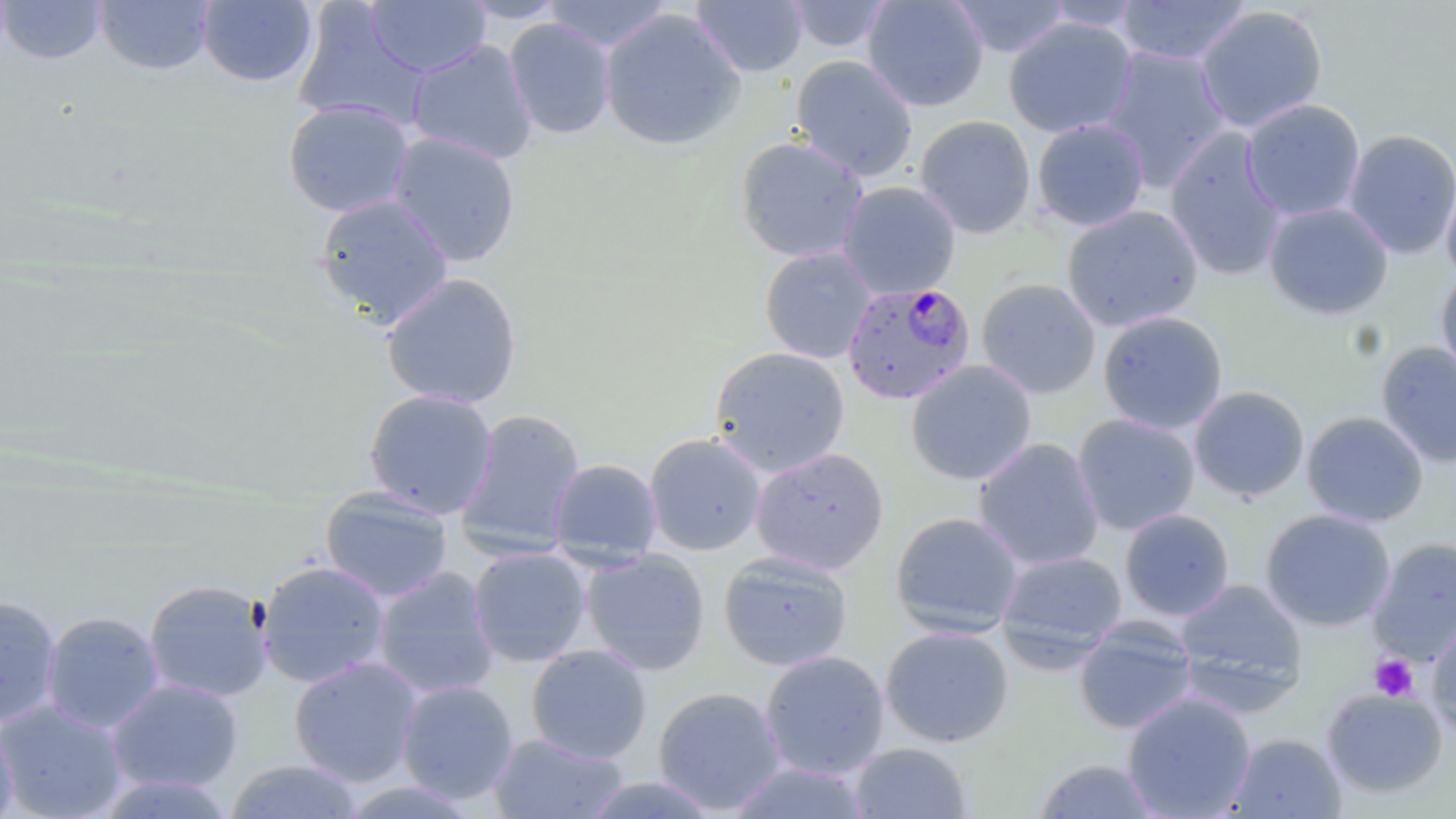 Approximate bounding boxes as (x1, y1, x2, y2) in pixels. Uninfected red blood cell locations: (0, 0, 107, 65), (458, 0, 569, 23), (542, 0, 673, 52), (692, 0, 808, 77), (786, 0, 893, 53), (862, 0, 989, 112), (947, 0, 1072, 58), (1115, 0, 1252, 66), (93, 1, 215, 75), (196, 1, 319, 88), (364, 1, 490, 78), (1041, 1, 1146, 32), (292, 3, 428, 131), (1194, 4, 1329, 133), (599, 7, 746, 151), (1003, 17, 1138, 139), (504, 18, 617, 139), (406, 39, 538, 165), (1098, 46, 1230, 190), (790, 55, 918, 182), (1241, 98, 1366, 222), (282, 99, 414, 217), (915, 114, 1036, 239), (1031, 118, 1150, 232), (1164, 128, 1288, 281), (1342, 129, 1456, 259), (385, 130, 522, 267), (734, 135, 870, 263), (1440, 173, 1456, 287), (837, 181, 961, 300), (313, 193, 455, 329), (1263, 201, 1394, 320), (1061, 205, 1204, 332), (759, 246, 877, 364), (1436, 270, 1456, 385), (381, 272, 523, 409), (976, 278, 1101, 399), (1097, 310, 1228, 434), (1375, 341, 1456, 468), (709, 346, 850, 478), (905, 360, 1037, 485), (1189, 386, 1309, 501), (362, 388, 499, 518), (455, 408, 587, 557), (1301, 411, 1429, 528), (1072, 413, 1201, 536), (643, 432, 767, 556), (973, 437, 1105, 571), (750, 447, 889, 575), (548, 458, 663, 567), (319, 487, 454, 603), (1119, 508, 1235, 621), (1259, 508, 1396, 632), (889, 511, 1024, 638), (1368, 537, 1456, 664), (468, 546, 592, 667), (996, 549, 1128, 664), (580, 550, 711, 676), (718, 550, 854, 672), (255, 560, 391, 689), (371, 567, 500, 700), (143, 578, 274, 703), (1174, 578, 1308, 705), (0, 594, 63, 728), (41, 610, 165, 734), (1426, 616, 1456, 739), (1073, 618, 1198, 735), (879, 625, 1014, 747), (525, 645, 652, 764), (759, 650, 890, 780), (288, 655, 423, 787), (105, 677, 244, 794), (396, 679, 519, 804), (653, 686, 786, 814), (1321, 687, 1449, 798), (1121, 690, 1256, 819), (0, 699, 128, 819), (0, 721, 18, 819), (489, 732, 628, 819), (1224, 732, 1347, 818), (848, 742, 973, 818), (1033, 758, 1162, 818), (226, 759, 365, 819), (728, 761, 871, 818), (96, 772, 236, 818), (582, 774, 721, 818). Plasmodium falciparum-infected red blood cell locations: (842, 281, 976, 405). Platelet locations: (1370, 654, 1418, 702). Slide-level diagnosis: Plasmodium falciparum. Image is 1456×819 pixels. Thin blood smear. May-Grünwald-Giemsa-stained preparation. Single field of view. 1000x magnification. Light microscopy.